Report the malaria status of this cell.
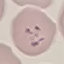

Parasitized.

preparation: thin blood smear
stain: Giemsa
capture: smartphone through the microscope eyepiece
image_type: automatically extracted cell patch, resized to 64 × 64 pixels